Identify the parasite.
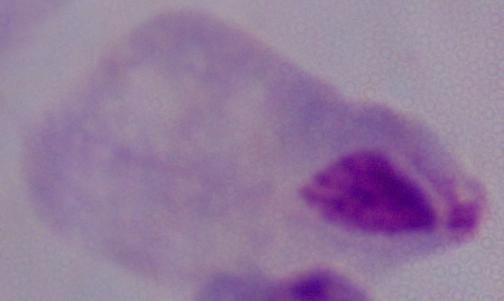
A trichomonad.

modality = micrograph
magnification = 1000x